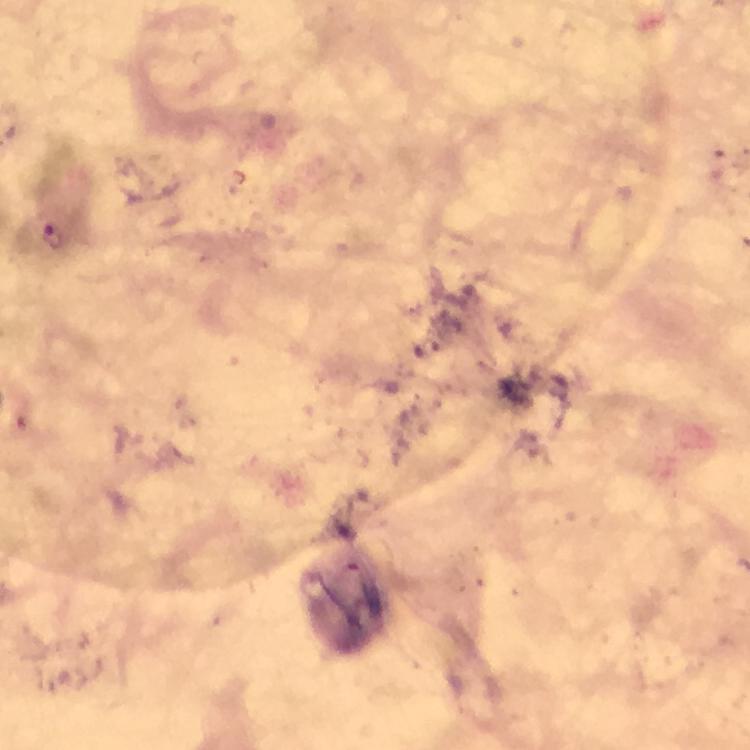 Approximate centers as {x, y} in pixels. Plasmodium parasite locations: {54, 234}. Thick blood film. At 100x magnification. Immersion oil applied. Smartphone photograph taken through a microscope. From a malaria diagnostic workup. A crop from one field of view. Image is 750×750 pixels. Giemsa stain.